Identify the preparation type.
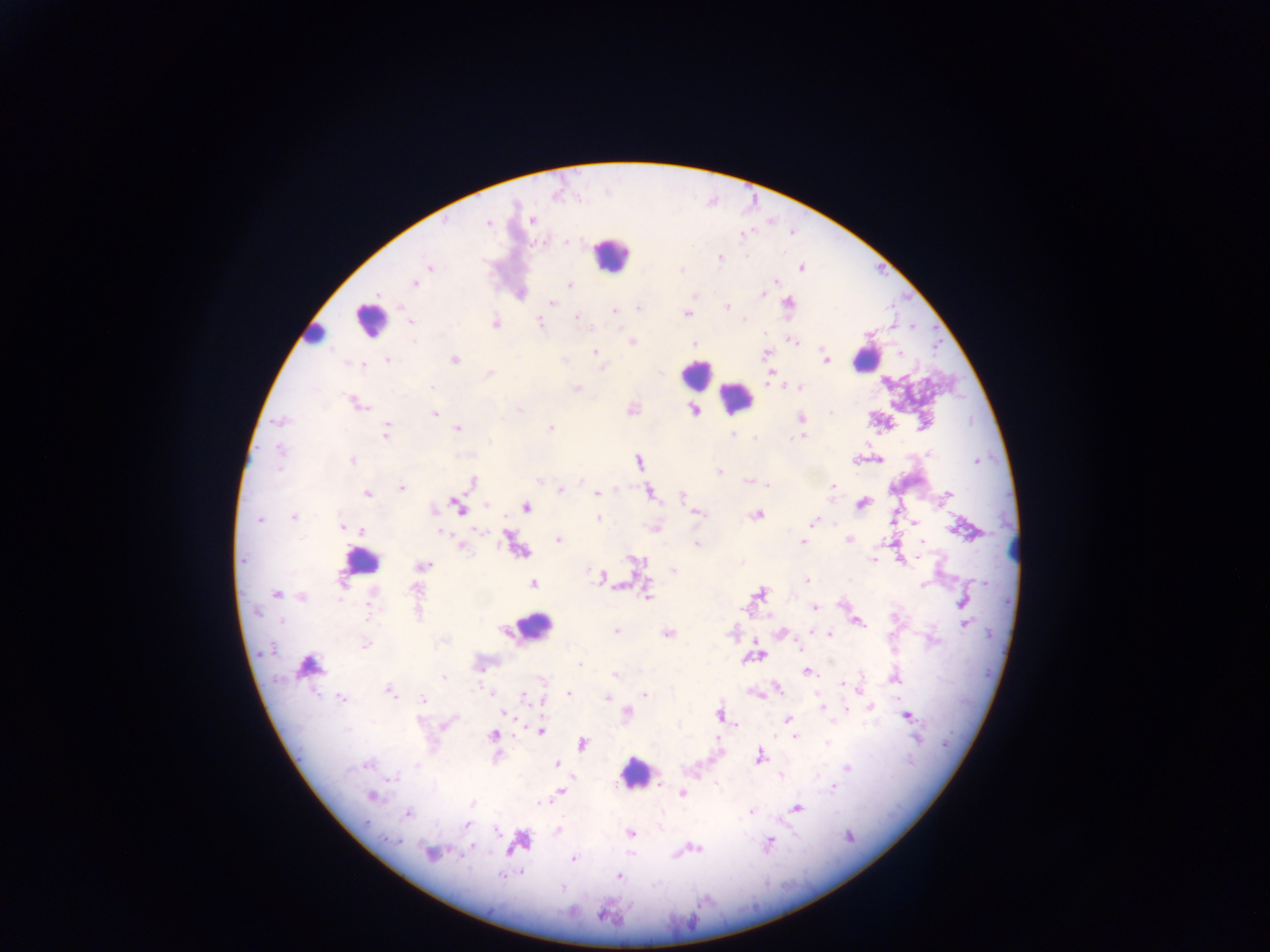
This is a thick smear.

Approximate centers as x y in pixels.
Summary:
  - Leukocyte locations: 610 254; 369 319; 312 333; 865 358; 695 374; 735 398; 361 561; 534 627; 635 773
  - Malaria parasite locations: 532 220; 488 223; 566 242; 720 258; 430 266; 801 268; 414 283; 569 284; 520 293; 763 294; 693 295; 552 303; 788 304; 638 306; 726 307; 614 311; 686 312; 576 316; 410 322; 495 322; 540 324; 632 342; 793 342; 693 344; 595 352; 765 353; 900 353; 386 359; 453 359; 826 360; 360 363; 772 370; 488 374; 799 387; 576 389; 356 404; 631 408; 519 409; 693 409; 434 414; 801 417; 280 421; 550 427; 457 428; 386 430; 732 435; 803 435; 878 459; 352 460; 856 460; 639 461; 718 471; 581 480; 471 481; 748 481; 767 485; 400 488; 831 488; 560 490; 648 492; 366 493; 596 494; 682 495; 947 496; 862 503; 487 504; 457 506; 526 507; 433 510; 695 511; 757 513; 293 517; 258 518; 598 519; 813 522; 915 522; 343 527; 655 527; 963 529; 441 530; 361 531; 509 537; 849 538; 559 540; 922 541; 803 542; 697 544; 461 545; 522 551; 243 559; 872 559; 901 559; 635 561; 741 562; 422 565; 672 570; 601 577; 807 581; 533 584; 760 592; 276 593; 648 596; 301 597; 962 601; 814 607; 963 612; 857 621; 965 624; 615 631; 667 632; 779 633; 830 634; 365 644; 760 655; 743 660; 579 664; 308 666; 806 672; 615 675; 444 678; 892 679; 777 689; 858 689; 389 690; 567 693; 645 695; 607 697; 342 699; 423 700; 541 700; 821 707; 870 707; 845 709; 504 712; 626 713; 719 714; 906 715; 788 719; 444 724; 735 725; 540 731; 493 735; 795 736; 916 739; 582 744; 758 756; 557 763; 847 767; 779 774; 661 781; 832 787; 559 791; 682 793; 371 795; 471 804; 796 807; 750 811; 408 813; 467 824; 552 825; 630 833; 769 843; 696 847; 430 853; 568 855; 501 876; 619 876
  - Country: Ghana
  - Image size: 1270×952 pixels
  - Capture: mobile-phone photograph through a microscope
  - Field of view: single